Describe the morphology of the erythrocytes.
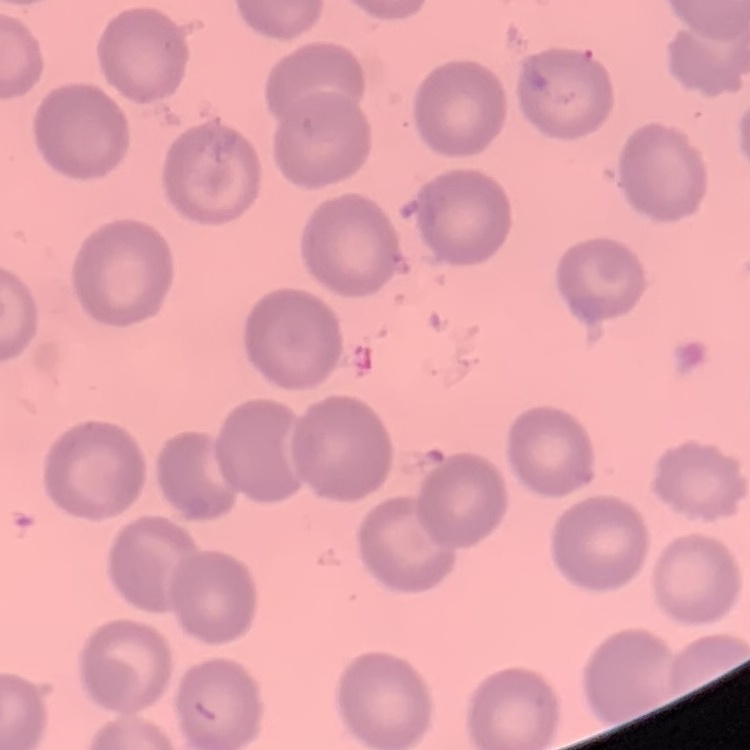
No rouleaux formation.

Thin blood smear. Square crop of a larger photomicrograph. Stained with either Field's or Giemsa.